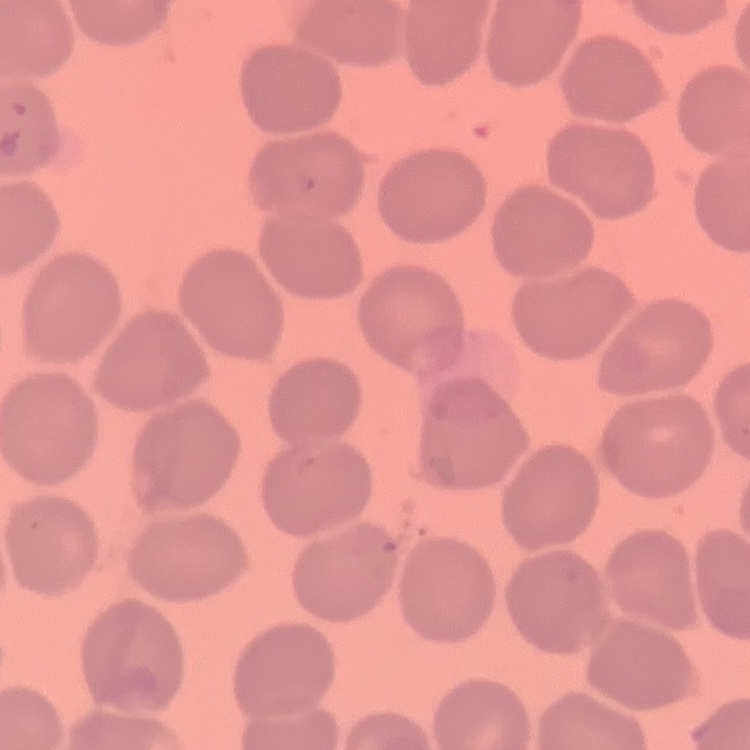
Summary:
  - Erythrocyte morphology: no rouleaux formation
  - Stain: Field's or Giemsa
  - Image type: one tile cut from a larger photomicrograph
  - Preparation: thin blood smear